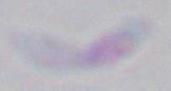
Captured at 1000x magnification. Toxoplasma gondii is shown. Micrograph.